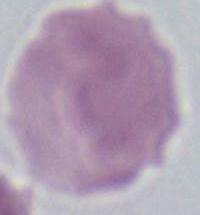

Summary:
  - Identification: erythrocyte
  - Magnification: 1000x
  - Modality: micrograph